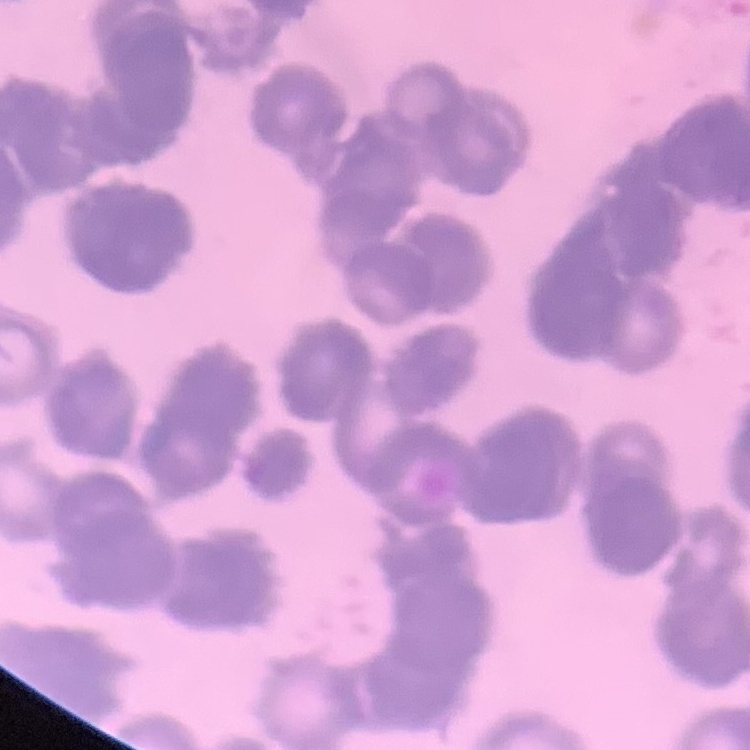

Summary:
  - Erythrocyte morphology: rouleaux formation
  - Stain: Field's or Giemsa
  - Preparation: thin blood film
  - Image type: one tile cut from a larger photomicrograph